State the blood parasite species.
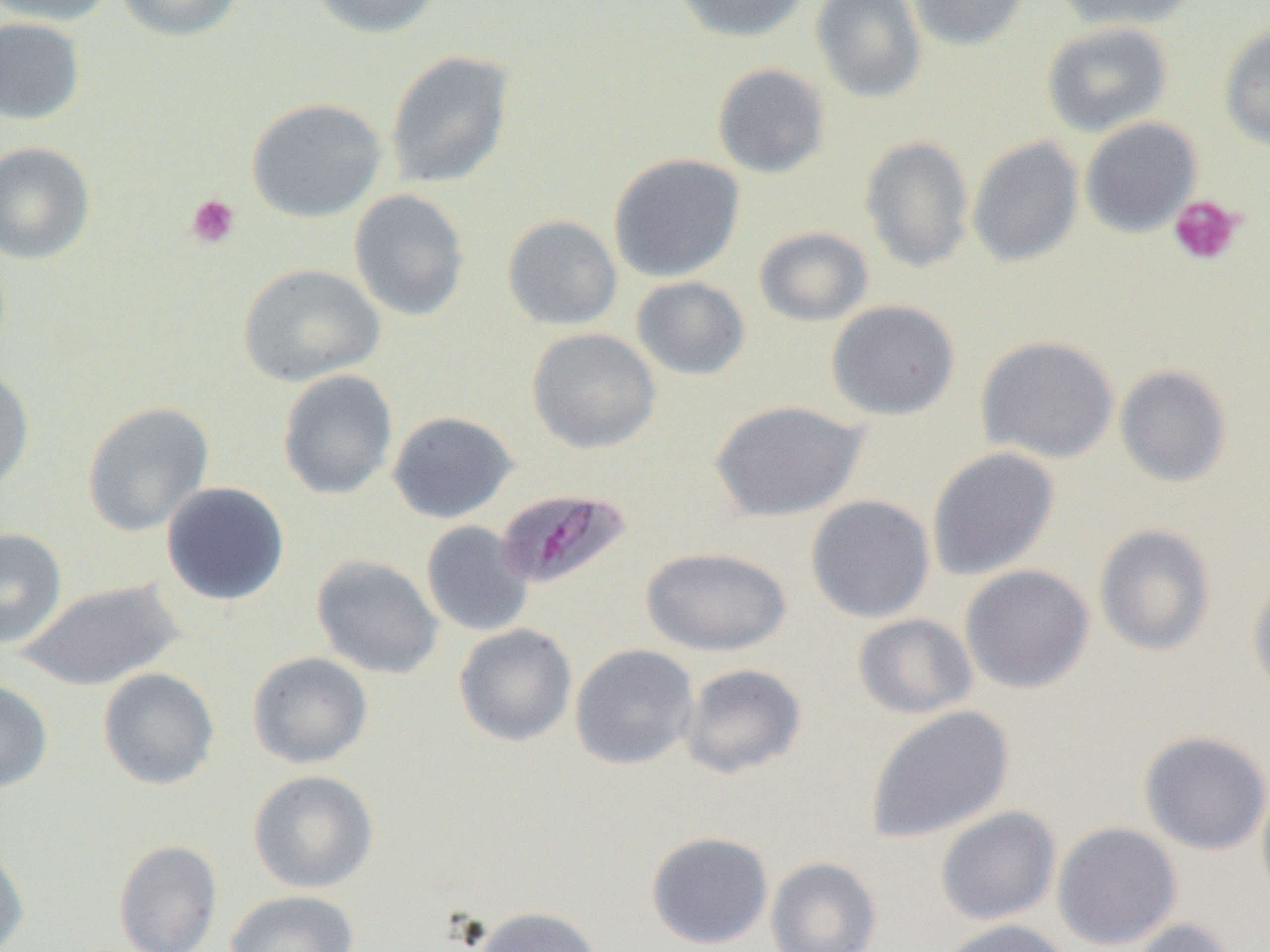
Plasmodium malariae.

Summary:
  - Coordinate format: approximate bounding boxes as named x1/y1/x2/y2 corners in pixels
  - Plasmodium malariae-infected red blood cell locations: (x1=494, y1=487, x2=632, y2=591)
  - Uninfected red blood cell locations: (x1=0, y1=0, x2=117, y2=26), (x1=115, y1=0, x2=245, y2=42), (x1=310, y1=0, x2=440, y2=38), (x1=673, y1=0, x2=810, y2=43), (x1=811, y1=0, x2=927, y2=103), (x1=907, y1=0, x2=1030, y2=50), (x1=1053, y1=0, x2=1199, y2=31), (x1=0, y1=16, x2=86, y2=125), (x1=1041, y1=21, x2=1173, y2=137), (x1=1218, y1=24, x2=1270, y2=150), (x1=384, y1=50, x2=516, y2=190), (x1=712, y1=63, x2=830, y2=178), (x1=247, y1=97, x2=387, y2=222), (x1=1079, y1=117, x2=1202, y2=238), (x1=859, y1=135, x2=974, y2=273), (x1=966, y1=136, x2=1084, y2=267), (x1=0, y1=141, x2=96, y2=264), (x1=608, y1=153, x2=746, y2=283), (x1=349, y1=189, x2=470, y2=321), (x1=502, y1=214, x2=623, y2=331), (x1=754, y1=226, x2=874, y2=327), (x1=238, y1=262, x2=385, y2=387), (x1=630, y1=275, x2=751, y2=380), (x1=826, y1=299, x2=960, y2=421), (x1=526, y1=327, x2=661, y2=454), (x1=976, y1=335, x2=1120, y2=463), (x1=0, y1=364, x2=35, y2=495), (x1=1114, y1=364, x2=1233, y2=487), (x1=277, y1=369, x2=399, y2=499), (x1=708, y1=399, x2=869, y2=522), (x1=82, y1=401, x2=214, y2=536), (x1=387, y1=410, x2=518, y2=523), (x1=926, y1=446, x2=1060, y2=580), (x1=161, y1=482, x2=290, y2=605), (x1=805, y1=494, x2=935, y2=623), (x1=420, y1=520, x2=534, y2=637), (x1=1094, y1=524, x2=1216, y2=656), (x1=0, y1=528, x2=67, y2=648), (x1=640, y1=546, x2=793, y2=655), (x1=311, y1=554, x2=443, y2=680), (x1=959, y1=564, x2=1094, y2=694), (x1=1247, y1=575, x2=1270, y2=697), (x1=17, y1=578, x2=186, y2=691), (x1=853, y1=613, x2=978, y2=720), (x1=453, y1=623, x2=577, y2=746), (x1=570, y1=643, x2=699, y2=769), (x1=247, y1=651, x2=373, y2=769), (x1=678, y1=663, x2=807, y2=778), (x1=98, y1=667, x2=220, y2=790), (x1=0, y1=679, x2=53, y2=793), (x1=865, y1=704, x2=1014, y2=844), (x1=1138, y1=730, x2=1270, y2=855), (x1=248, y1=769, x2=379, y2=893), (x1=1256, y1=780, x2=1270, y2=910), (x1=935, y1=806, x2=1061, y2=925), (x1=1052, y1=822, x2=1182, y2=950), (x1=645, y1=831, x2=774, y2=949), (x1=0, y1=838, x2=29, y2=952), (x1=113, y1=839, x2=223, y2=952), (x1=765, y1=856, x2=882, y2=952), (x1=225, y1=890, x2=360, y2=952), (x1=471, y1=906, x2=604, y2=952), (x1=935, y1=918, x2=1077, y2=952), (x1=1126, y1=918, x2=1241, y2=952)
  - Platelet locations: (x1=186, y1=194, x2=240, y2=249), (x1=1169, y1=195, x2=1244, y2=266)
  - Preparation: thin blood smear
  - Field of view: one of a larger specimen
  - Magnification: 1000x
  - Image size: 1270×952 pixels
  - Modality: optical microscopy